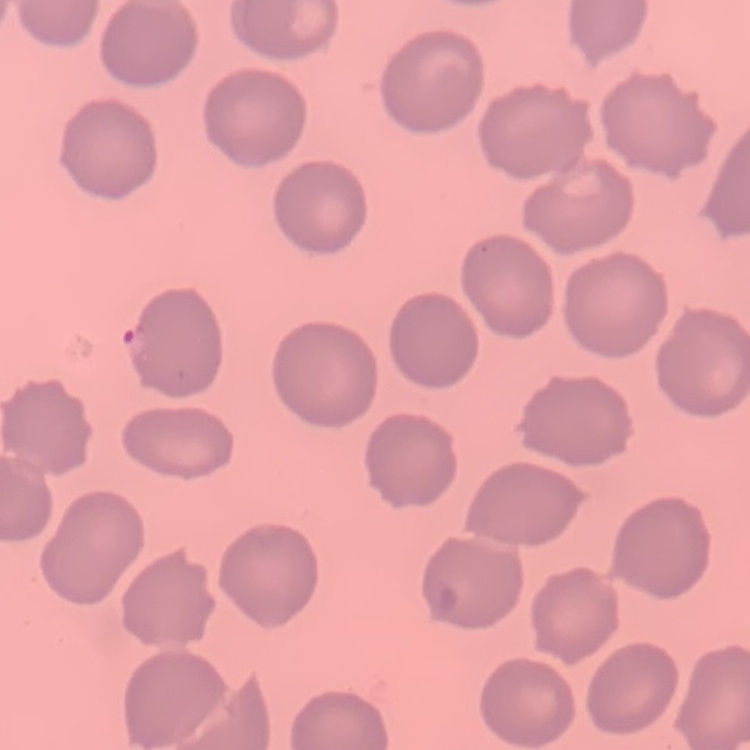

Summary:
  - Red blood cell morphology: no rouleaux formation
  - Image type: square crop of a larger photomicrograph
  - Stain: Field's or Giemsa
  - Preparation: thin blood film